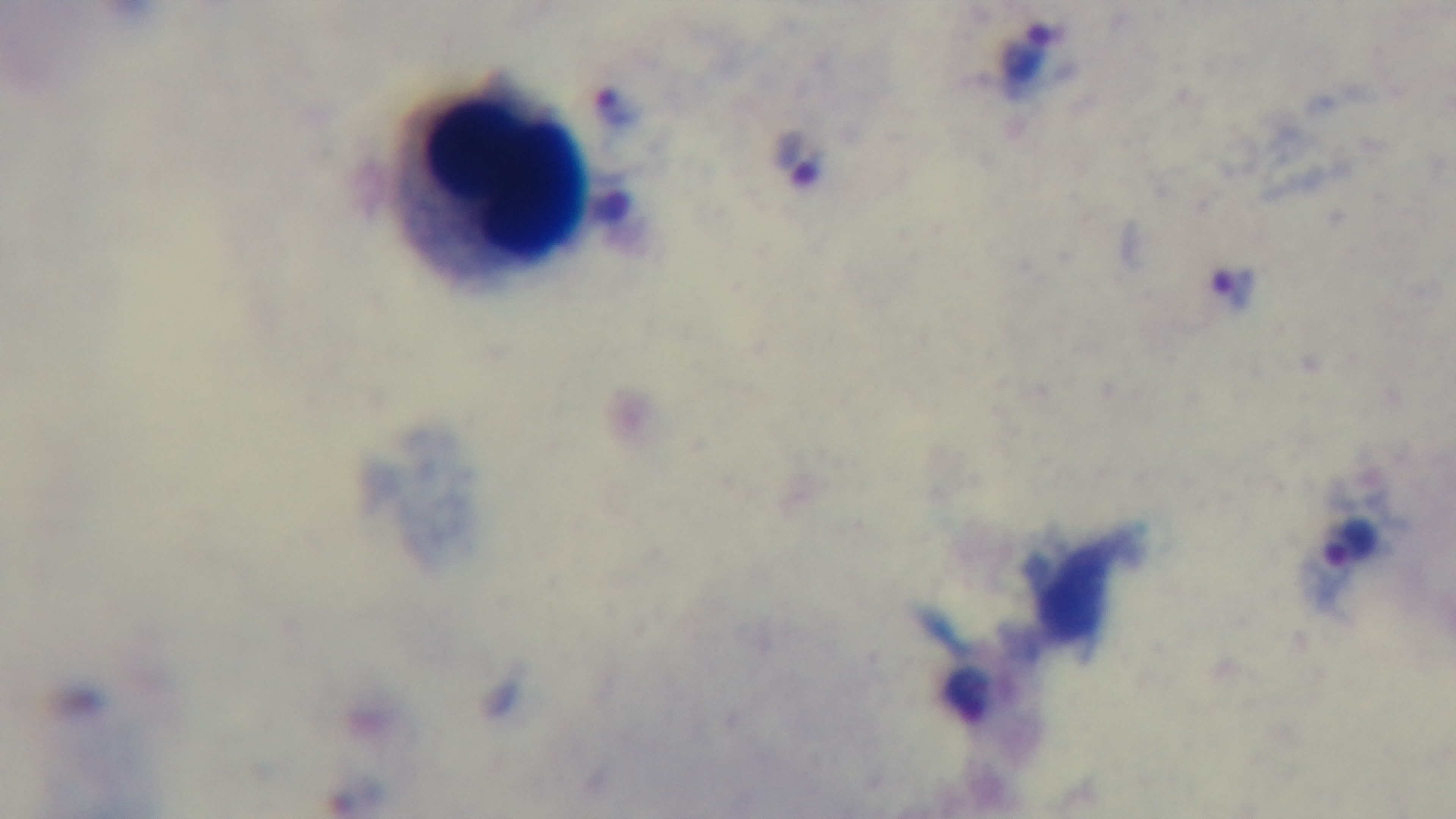

Summary:
  - Preparation: thick blood film
  - Objective: 100x oil immersion
  - Modality: light microscopy
  - Malaria status: infected
  - Capture: mounted 4K digital camera
  - Field of view: one from the slide
  - Stain: Giemsa